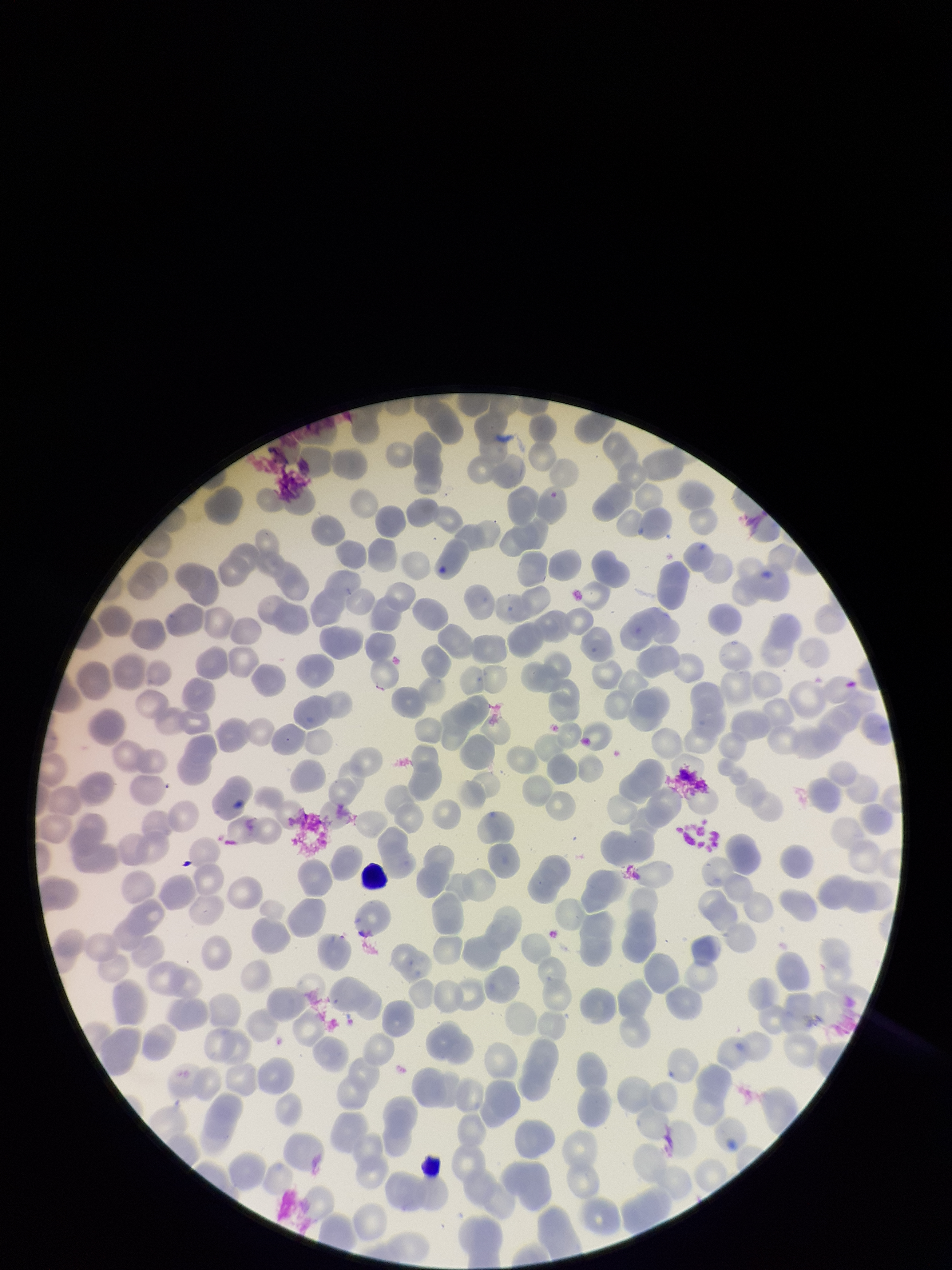
Summary:
  - Field of view: single
  - Preparation: thin
  - Stain: Giemsa
  - Image size: 952×1270 pixels
  - Parasitized red blood cells: none identified
  - Patient malaria status: negative
  - Parasitized red blood cell count: 0
  - Red blood cell count: 269
  - Capture: smartphone photograph through the microscope eyepiece